Name the parasite shown.
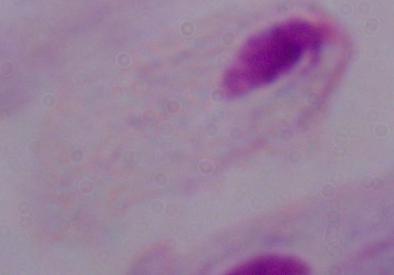
A trichomonad.

modality = micrograph
magnification = 1000x